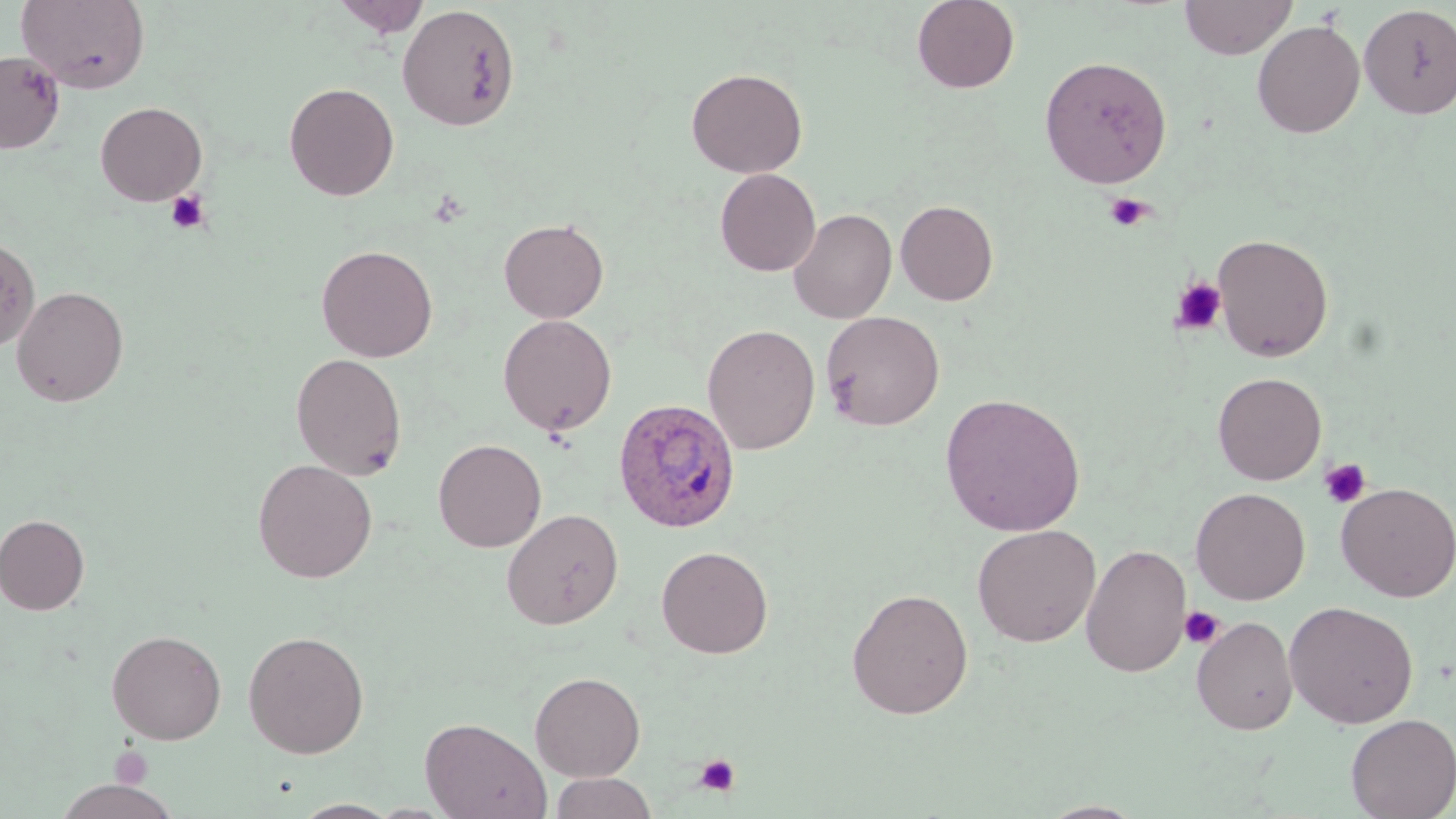 Approximate bounding boxes as (x1, y1, x2, y2) in pixels. Uninfected red blood cell locations: (16, 0, 151, 94), (331, 0, 431, 38), (911, 0, 1020, 94), (1180, 0, 1297, 59), (397, 4, 520, 131), (1358, 4, 1456, 119), (1252, 19, 1365, 138), (0, 50, 65, 153), (1039, 56, 1173, 188), (686, 67, 808, 178), (283, 82, 399, 201), (95, 101, 207, 206), (715, 168, 821, 276), (895, 199, 999, 306), (788, 208, 897, 324), (498, 218, 609, 323), (1212, 233, 1334, 362), (315, 244, 438, 362), (11, 285, 129, 407), (820, 310, 945, 431), (497, 314, 617, 436), (702, 323, 821, 455), (290, 352, 408, 480), (1212, 371, 1327, 485), (940, 392, 1086, 536), (433, 438, 546, 552), (252, 458, 377, 583), (1335, 481, 1456, 602), (1190, 487, 1310, 604), (500, 508, 624, 630), (0, 514, 90, 615), (972, 524, 1101, 647), (1081, 543, 1192, 678), (656, 545, 773, 658), (846, 587, 974, 719), (1283, 600, 1419, 728), (1191, 615, 1298, 735), (106, 628, 227, 745), (242, 629, 370, 759), (529, 671, 645, 781), (1345, 713, 1456, 819), (420, 716, 551, 819), (549, 772, 658, 818), (51, 779, 180, 819), (1035, 801, 1150, 818). Platelet locations: (165, 190, 211, 235), (1105, 192, 1152, 231), (1171, 278, 1226, 335), (1319, 458, 1371, 509), (1179, 605, 1224, 649), (109, 747, 152, 789), (694, 753, 741, 798). Plasmodium ovale-infected red blood cell locations: (613, 397, 741, 533). Slide-level diagnosis: Plasmodium ovale. Thin blood smear. Captured at 1000x magnification. One field of a larger specimen. Light microscopy. May-Grünwald-Giemsa stain. Image is 1456×819 pixels.